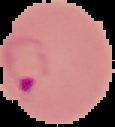
result = malaria parasites identified
image size = 115×127 pixels
preparation = thin blood film
image type = segmented cell region on a black background